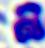 A white blood cell is shown. Captured at 400x magnification. Micrograph.